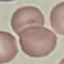

{
  "result": "no malaria parasites seen",
  "capture": "smartphone through the microscope eyepiece",
  "stain": "Giemsa",
  "image_type": "automatically extracted cell patch, resized to 64 × 64 pixels",
  "preparation": "thin blood film"
}